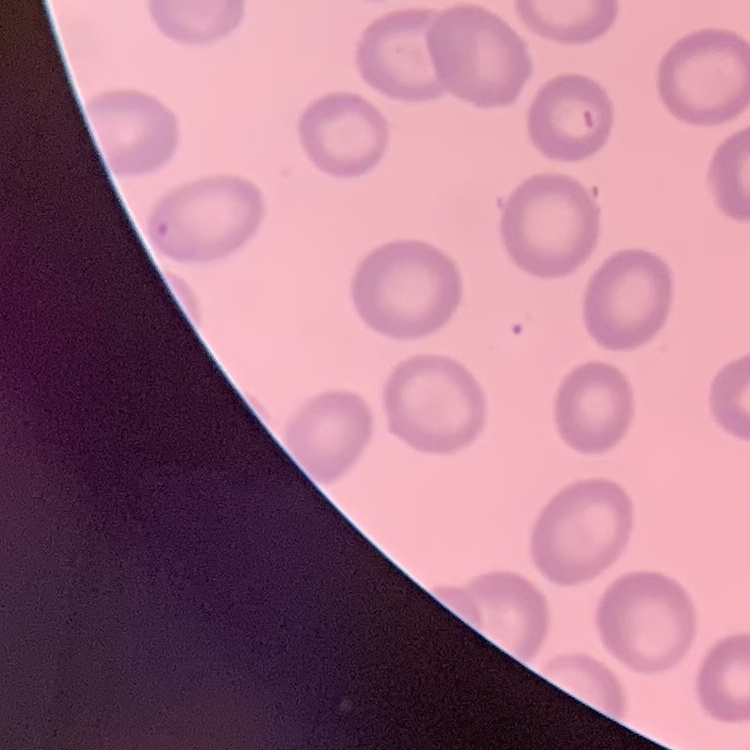 The erythrocytes show no rouleaux formation. Thin blood film. One tile cut from a larger photomicrograph. Stained with either Field's or Giemsa.